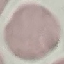
Summary:
  - Result: no malaria parasites seen
  - Capture: smartphone through the microscope eyepiece
  - Stain: Giemsa
  - Image type: automatically extracted cell patch, resized to 64 × 64 pixels
  - Preparation: thin smear